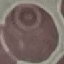

Result: no malaria parasites seen. Giemsa-stained preparation. Photographed with a smartphone camera at the microscope eyepiece. Thin smear of blood. Automatically extracted cell patch, resized to 64 × 64 pixels.